Assess this cell for malaria.
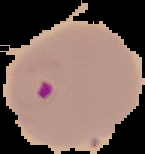

Parasitized.

Summary:
  - Preparation: thin blood film
  - Image type: segmented cell region with the area outside set to black
  - Image size: 145×154 pixels